Assess this cell for malaria.
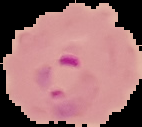
Parasitized.

{
  "preparation": "thin blood smear",
  "image_type": "cell region segmented out of the field of view; surrounding area masked to black",
  "image_size": "142×127 pixels"
}